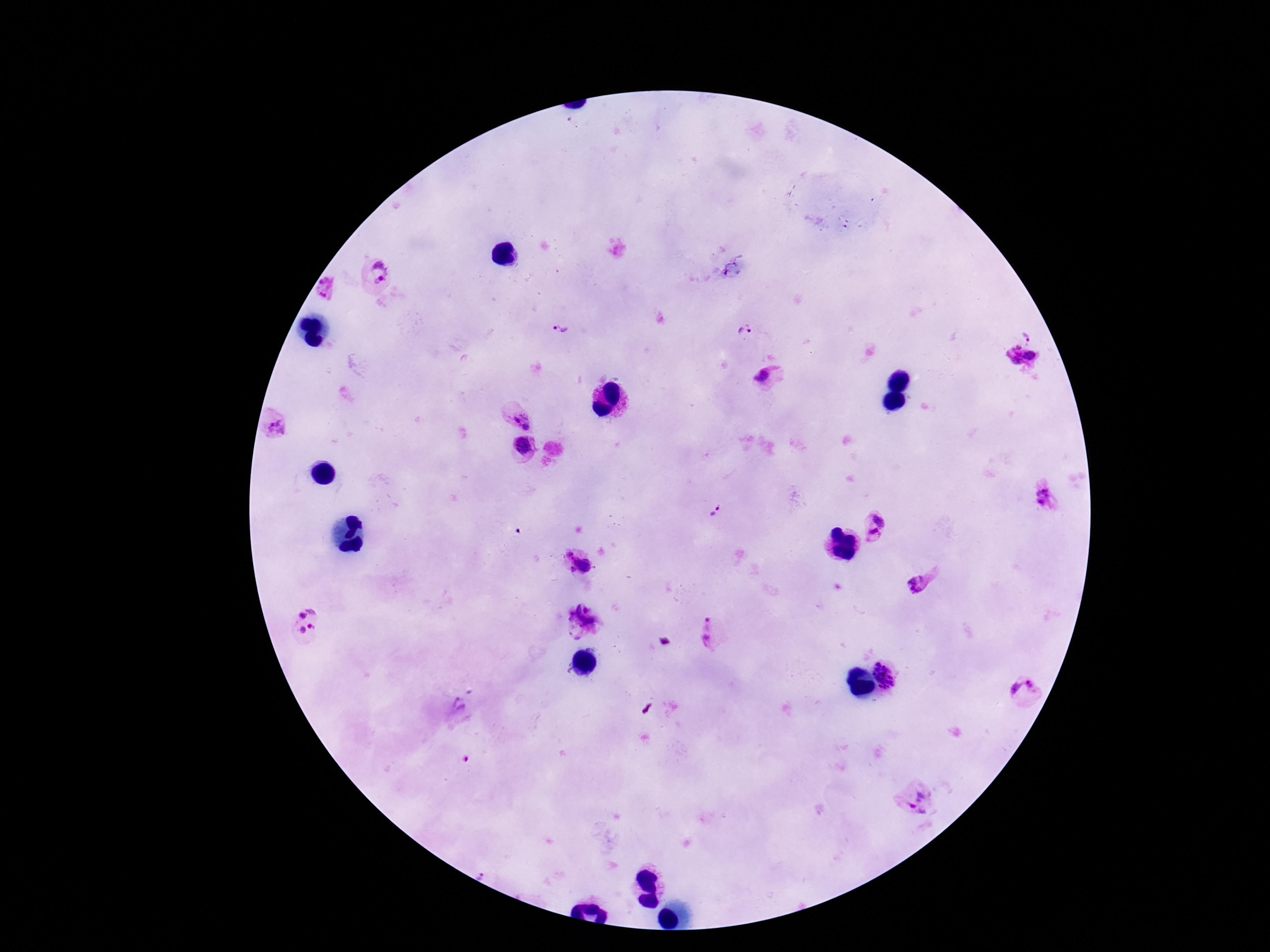

Approximate centers as [x, y] in pixels. Plasmodium parasite locations: [375, 275], [326, 287], [560, 329], [746, 332], [1028, 333], [1022, 356], [768, 377], [522, 419], [274, 425], [523, 445], [1046, 497], [715, 512], [879, 519], [874, 536], [579, 560], [919, 585], [304, 621], [583, 623], [707, 630], [893, 668], [1024, 690], [456, 706], [918, 801]. Patient malaria status: infected. Thick blood film. Image is 1270×952 pixels. One field from this slide. Smartphone photograph taken through the microscope eyepiece. 100x magnification. Giemsa stain.